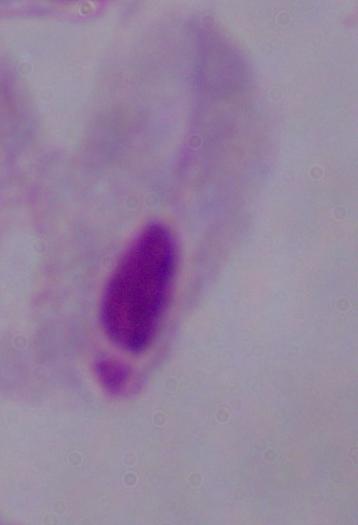
Summary:
  - Identification: trichomonad
  - Magnification: 1000x
  - Modality: micrograph